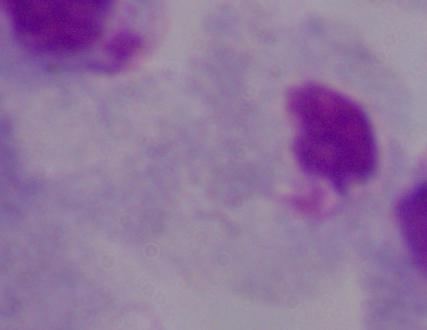

identification: trichomonad
modality: photomicrograph
magnification: 1000x